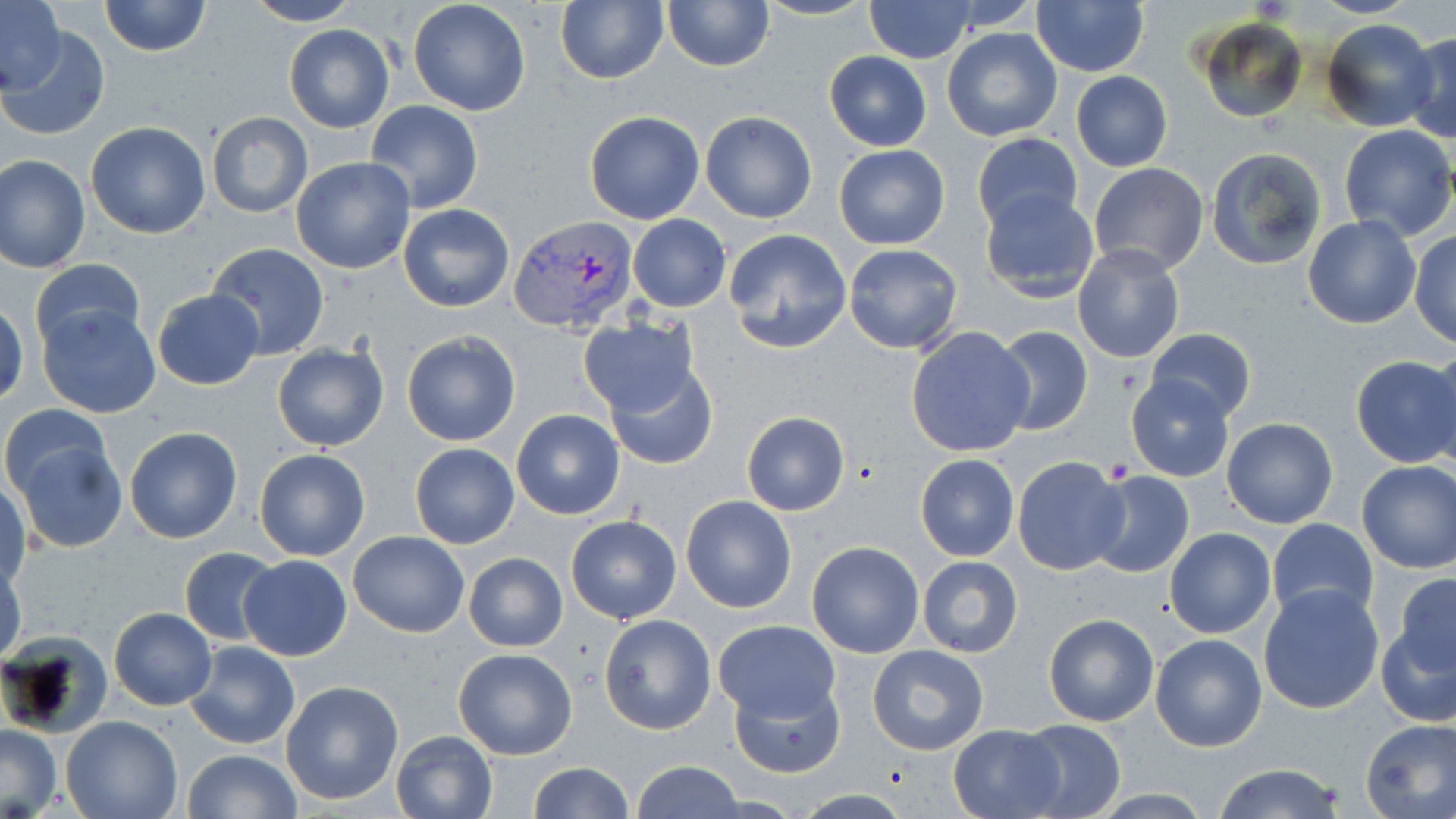 Approximate bounding boxes as named x1/y1/x2/y2 corners in pixels. Plasmodium vivax-infected red blood cell locations: (x1=509, y1=215, x2=638, y2=333). Platelet locations: (x1=1105, y1=458, x2=1133, y2=482). Uninfected red blood cell locations: (x1=98, y1=0, x2=211, y2=58), (x1=242, y1=0, x2=364, y2=26), (x1=556, y1=0, x2=668, y2=84), (x1=662, y1=0, x2=775, y2=72), (x1=755, y1=0, x2=877, y2=20), (x1=1030, y1=0, x2=1149, y2=76), (x1=1, y1=1, x2=63, y2=93), (x1=407, y1=1, x2=531, y2=117), (x1=864, y1=1, x2=975, y2=63), (x1=1197, y1=17, x2=1306, y2=124), (x1=1320, y1=18, x2=1438, y2=132), (x1=4, y1=25, x2=110, y2=140), (x1=284, y1=25, x2=395, y2=132), (x1=943, y1=28, x2=1062, y2=141), (x1=1403, y1=31, x2=1456, y2=143), (x1=824, y1=51, x2=931, y2=151), (x1=1070, y1=71, x2=1173, y2=173), (x1=364, y1=100, x2=484, y2=212), (x1=699, y1=110, x2=818, y2=223), (x1=206, y1=111, x2=312, y2=219), (x1=584, y1=111, x2=706, y2=225), (x1=85, y1=121, x2=211, y2=239), (x1=1337, y1=124, x2=1455, y2=242), (x1=971, y1=132, x2=1085, y2=236), (x1=834, y1=144, x2=949, y2=250), (x1=1205, y1=147, x2=1329, y2=273), (x1=1, y1=155, x2=90, y2=274), (x1=292, y1=156, x2=417, y2=273), (x1=1089, y1=162, x2=1210, y2=277), (x1=979, y1=188, x2=1102, y2=302), (x1=397, y1=202, x2=515, y2=312), (x1=627, y1=215, x2=732, y2=312), (x1=1302, y1=216, x2=1421, y2=329), (x1=1409, y1=228, x2=1456, y2=349), (x1=722, y1=229, x2=853, y2=354), (x1=204, y1=241, x2=331, y2=360), (x1=843, y1=243, x2=963, y2=354), (x1=1073, y1=247, x2=1184, y2=364), (x1=28, y1=257, x2=144, y2=355), (x1=152, y1=288, x2=264, y2=391), (x1=0, y1=302, x2=27, y2=406), (x1=37, y1=302, x2=162, y2=418), (x1=575, y1=316, x2=701, y2=417), (x1=992, y1=325, x2=1093, y2=437), (x1=905, y1=327, x2=1036, y2=457), (x1=1147, y1=329, x2=1255, y2=422), (x1=402, y1=331, x2=520, y2=447), (x1=1433, y1=341, x2=1456, y2=466), (x1=272, y1=342, x2=389, y2=452), (x1=1351, y1=354, x2=1456, y2=468), (x1=603, y1=362, x2=720, y2=471), (x1=1126, y1=377, x2=1234, y2=483), (x1=2, y1=402, x2=112, y2=505), (x1=512, y1=409, x2=625, y2=520), (x1=741, y1=412, x2=849, y2=516), (x1=1222, y1=417, x2=1338, y2=529), (x1=124, y1=425, x2=243, y2=544), (x1=11, y1=435, x2=128, y2=553), (x1=410, y1=443, x2=519, y2=548), (x1=254, y1=449, x2=372, y2=562), (x1=914, y1=453, x2=1020, y2=561), (x1=1012, y1=456, x2=1128, y2=575), (x1=1356, y1=460, x2=1456, y2=574), (x1=1086, y1=470, x2=1195, y2=579), (x1=1, y1=480, x2=30, y2=588), (x1=680, y1=495, x2=797, y2=613), (x1=565, y1=514, x2=682, y2=623), (x1=1266, y1=519, x2=1379, y2=626), (x1=1165, y1=528, x2=1277, y2=639), (x1=348, y1=530, x2=469, y2=637), (x1=806, y1=540, x2=925, y2=658), (x1=180, y1=546, x2=282, y2=646), (x1=463, y1=552, x2=568, y2=652), (x1=0, y1=555, x2=27, y2=667), (x1=239, y1=555, x2=352, y2=662), (x1=917, y1=555, x2=1024, y2=657), (x1=1392, y1=574, x2=1456, y2=677), (x1=1258, y1=585, x2=1385, y2=715), (x1=108, y1=608, x2=216, y2=710), (x1=1043, y1=611, x2=1160, y2=727), (x1=599, y1=613, x2=717, y2=735), (x1=1377, y1=613, x2=1456, y2=729), (x1=713, y1=618, x2=839, y2=723), (x1=1150, y1=633, x2=1267, y2=752), (x1=2, y1=634, x2=112, y2=737), (x1=184, y1=640, x2=301, y2=750), (x1=867, y1=644, x2=989, y2=754), (x1=453, y1=646, x2=579, y2=761), (x1=279, y1=679, x2=405, y2=806), (x1=731, y1=680, x2=845, y2=779), (x1=60, y1=716, x2=181, y2=819), (x1=1359, y1=717, x2=1456, y2=818), (x1=1013, y1=719, x2=1125, y2=819), (x1=0, y1=724, x2=62, y2=817), (x1=948, y1=724, x2=1064, y2=818), (x1=390, y1=728, x2=499, y2=819), (x1=181, y1=749, x2=301, y2=819), (x1=634, y1=761, x2=743, y2=818), (x1=530, y1=762, x2=633, y2=819), (x1=1212, y1=763, x2=1346, y2=819). Slide-level diagnosis: Plasmodium vivax. May-Grünwald-Giemsa-stained preparation. Single field of view. Captured at 1000x magnification. Optical microscopy. Thin blood film. Image is 1456×819 pixels.